Report the malaria status of this cell.
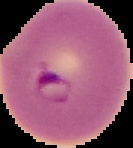
It is parasitized.

image_type: segmented cell region with the area outside set to black
image_size: 133×148 pixels
preparation: thin blood film